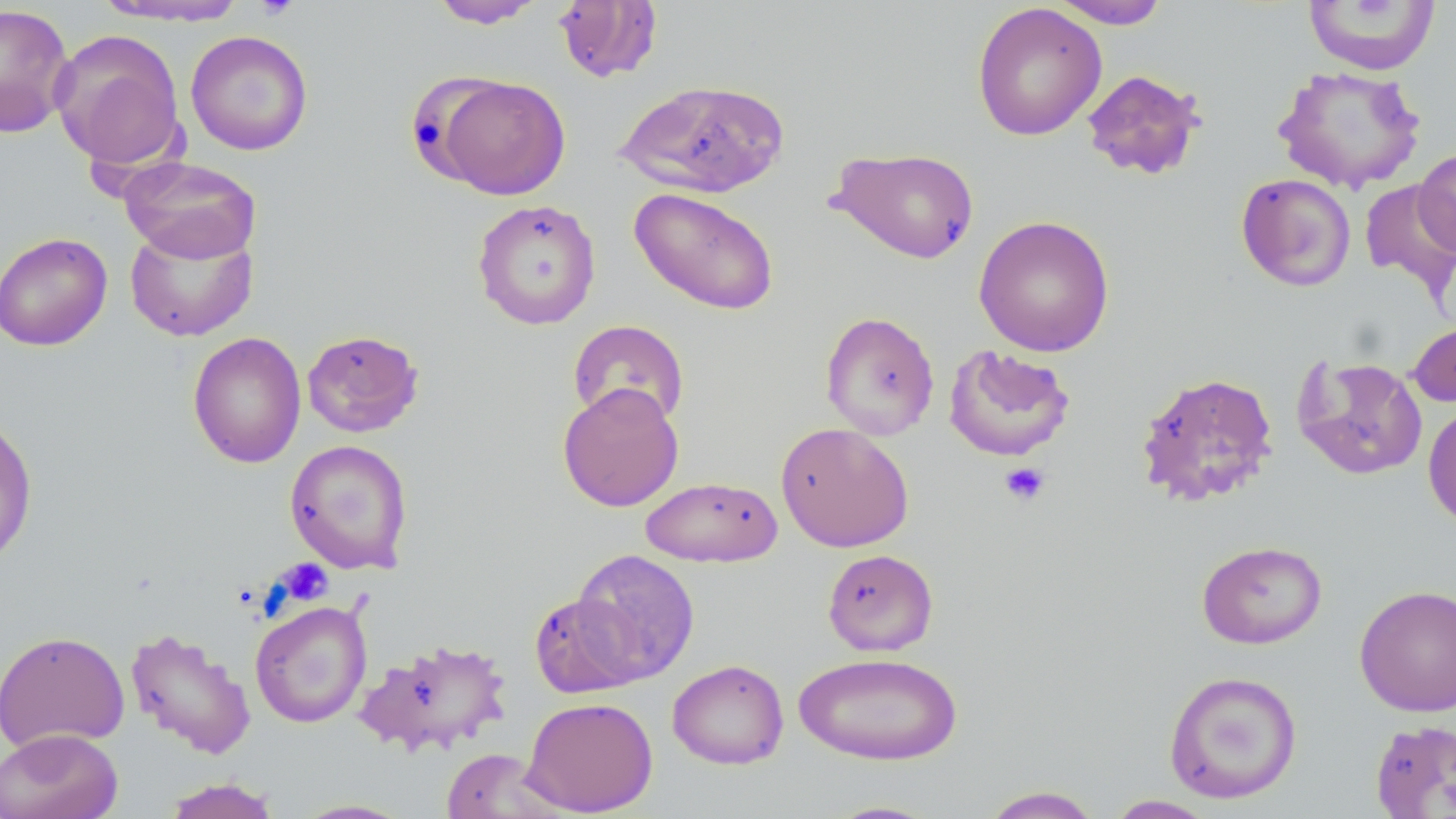

{
  "slide_level_diagnosis": "negative for blood parasites",
  "uninfected_red_blood_cell_locations": "approximate bounding boxes as [x1, y1, x2, y2] in pixels: [93, 0, 251, 26], [430, 0, 546, 29], [1048, 0, 1171, 29], [553, 1, 663, 83], [1303, 1, 1441, 75], [971, 2, 1107, 141], [0, 3, 75, 138], [49, 29, 186, 172], [185, 30, 314, 156], [1273, 64, 1427, 193], [1081, 69, 1207, 181], [433, 75, 571, 200], [409, 78, 512, 182], [616, 78, 789, 198], [830, 146, 980, 265], [1413, 147, 1456, 259], [119, 156, 261, 263], [1235, 173, 1357, 292], [1359, 179, 1456, 299], [629, 187, 780, 316], [472, 199, 601, 330], [973, 214, 1115, 357], [124, 223, 257, 342], [0, 231, 113, 351], [820, 310, 940, 441], [567, 319, 690, 428], [1408, 320, 1456, 409], [302, 329, 424, 437], [188, 331, 306, 469], [943, 344, 1076, 461], [1291, 353, 1429, 481], [1135, 370, 1279, 508], [557, 382, 684, 512], [1422, 400, 1456, 532], [0, 412, 38, 567], [775, 422, 914, 552], [284, 439, 414, 574], [640, 476, 782, 567], [1196, 540, 1327, 649], [570, 548, 701, 684], [822, 548, 938, 655], [1354, 584, 1456, 716], [528, 592, 642, 698], [250, 600, 372, 728], [125, 626, 256, 760], [0, 630, 130, 752], [356, 638, 513, 757], [794, 651, 963, 766], [667, 659, 789, 770], [1163, 669, 1303, 804], [521, 697, 658, 816], [1370, 719, 1456, 818], [0, 728, 123, 819], [440, 747, 563, 819], [161, 778, 283, 818], [980, 786, 1103, 818], [1105, 795, 1218, 818], [290, 798, 417, 818], [822, 799, 944, 818]",
  "field_of_view": "one of a larger specimen",
  "stain": "May-Grünwald-Giemsa",
  "image_size": "1456×819 pixels",
  "preparation": "thin blood smear",
  "modality": "light microscopy",
  "magnification": "1000x",
  "platelet_locations": "approximate bounding boxes as [x1, y1, x2, y2] in pixels: [254, 0, 299, 21], [999, 462, 1051, 507], [275, 558, 334, 606]"
}